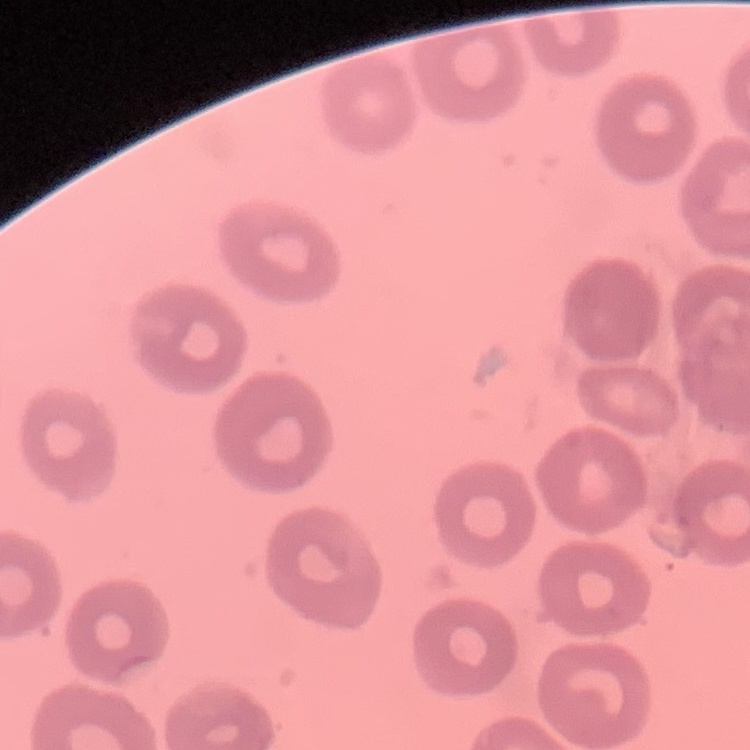
Summary:
  - Red blood cell morphology: no rouleaux formation
  - Image type: square crop of a larger photomicrograph
  - Preparation: thin blood smear
  - Stain: Field's or Giemsa